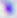

Summary:
  - Magnification: 400x
  - Identification: Toxoplasma gondii
  - Modality: photomicrograph